Report the malaria status of this cell.
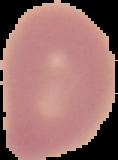
Uninfected.

Summary:
  - Image size: 118×160 pixels
  - Image type: cell region segmented out of the field of view; surrounding area masked to black
  - Preparation: thin blood smear